Identify the parasite.
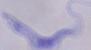
A trypanosome.

modality: photomicrograph
magnification: 1000x